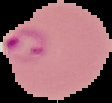
{
  "malaria_status": "parasitized",
  "image_size": "112×103 pixels",
  "image_type": "segmented cell region on a black background",
  "preparation": "thin blood smear"
}